Identify the preparation type.
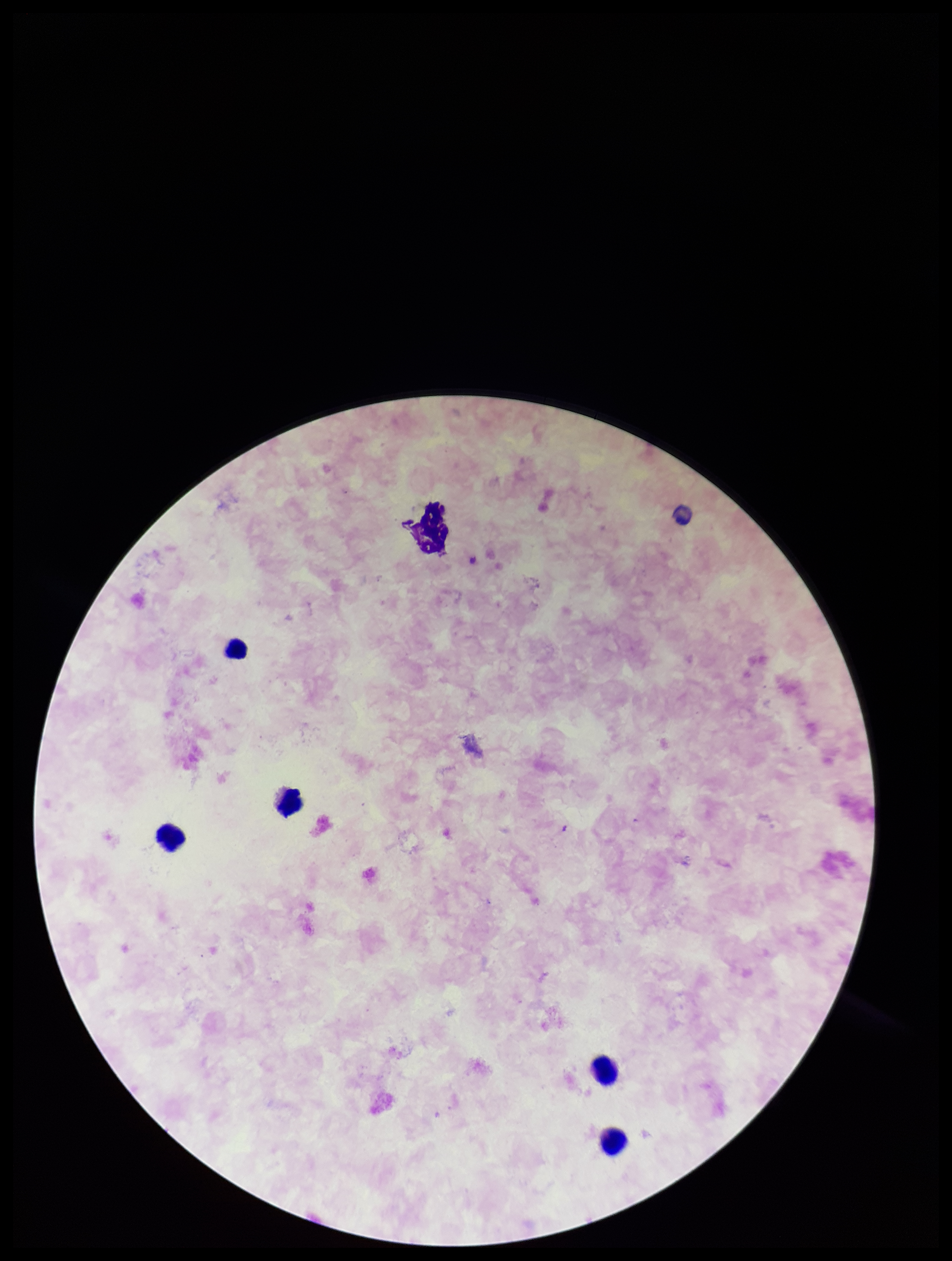
Thick.

image_size: 952×1261 pixels
parasite_count: 0
capture: smartphone photograph through the microscope eyepiece
field_of_view: one from this slide
stain: Giemsa
leukocyte_count: 5
plasmodium_parasites: none identified
patient_malaria_status: negative